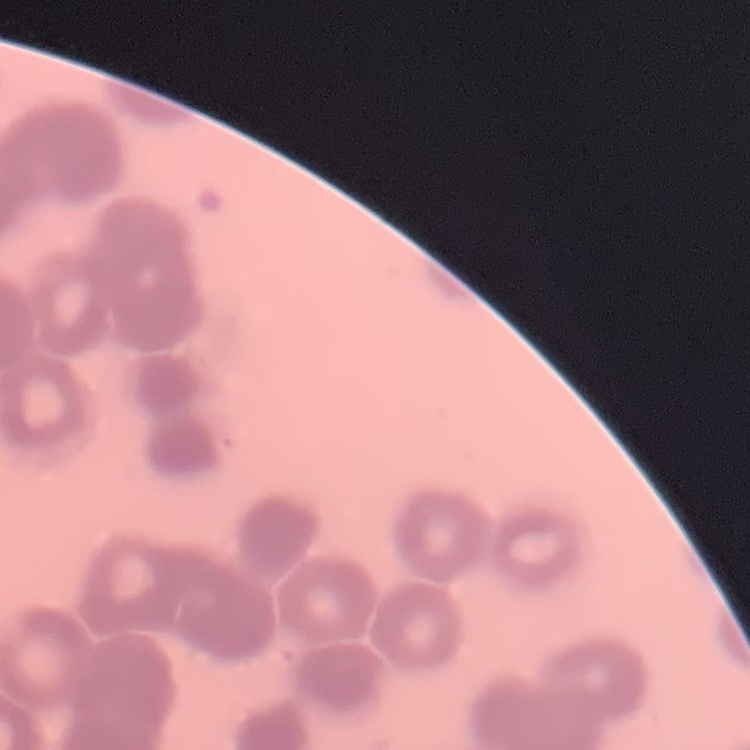
Summary:
  - Red blood cell morphology: rouleaux formation
  - Preparation: thin blood film
  - Stain: Field's or Giemsa
  - Image type: one tile cut from a larger photomicrograph